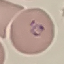

Summary:
  - Result: malaria parasites detected
  - Stain: Giemsa
  - Capture: smartphone through the microscope eyepiece
  - Image type: cell patch, automatically extracted from a larger field of view and resized to 64 × 64 pixels
  - Preparation: thin smear